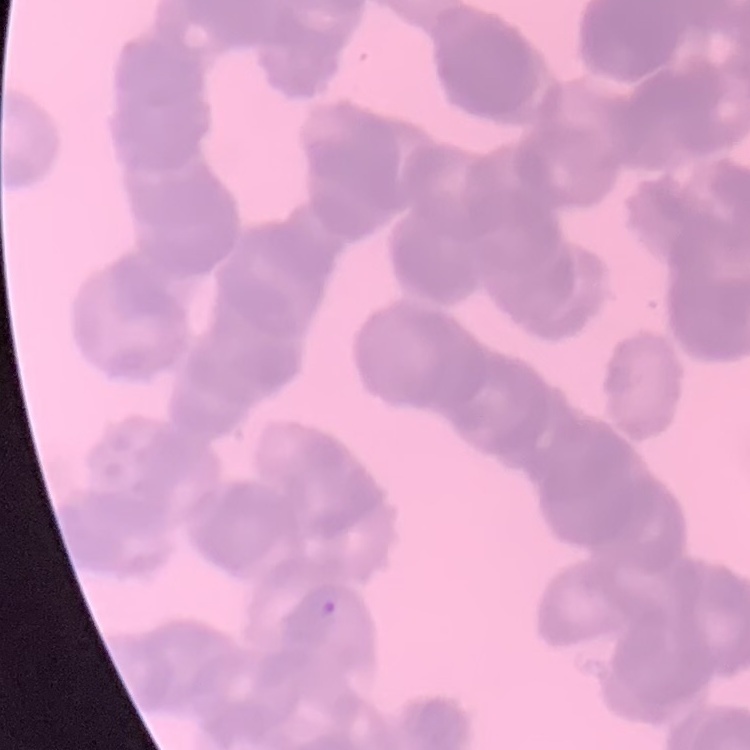
Summary:
  - Erythrocyte morphology: rouleaux formation
  - Preparation: thin blood smear
  - Stain: Field's or Giemsa
  - Image type: one tile cut from a larger photomicrograph